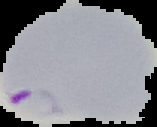

{
  "image_type": "segmented cell region on a black background",
  "image_size": "157×127 pixels",
  "malaria_status": "parasitized",
  "preparation": "thin blood film"
}